Locate platelets.
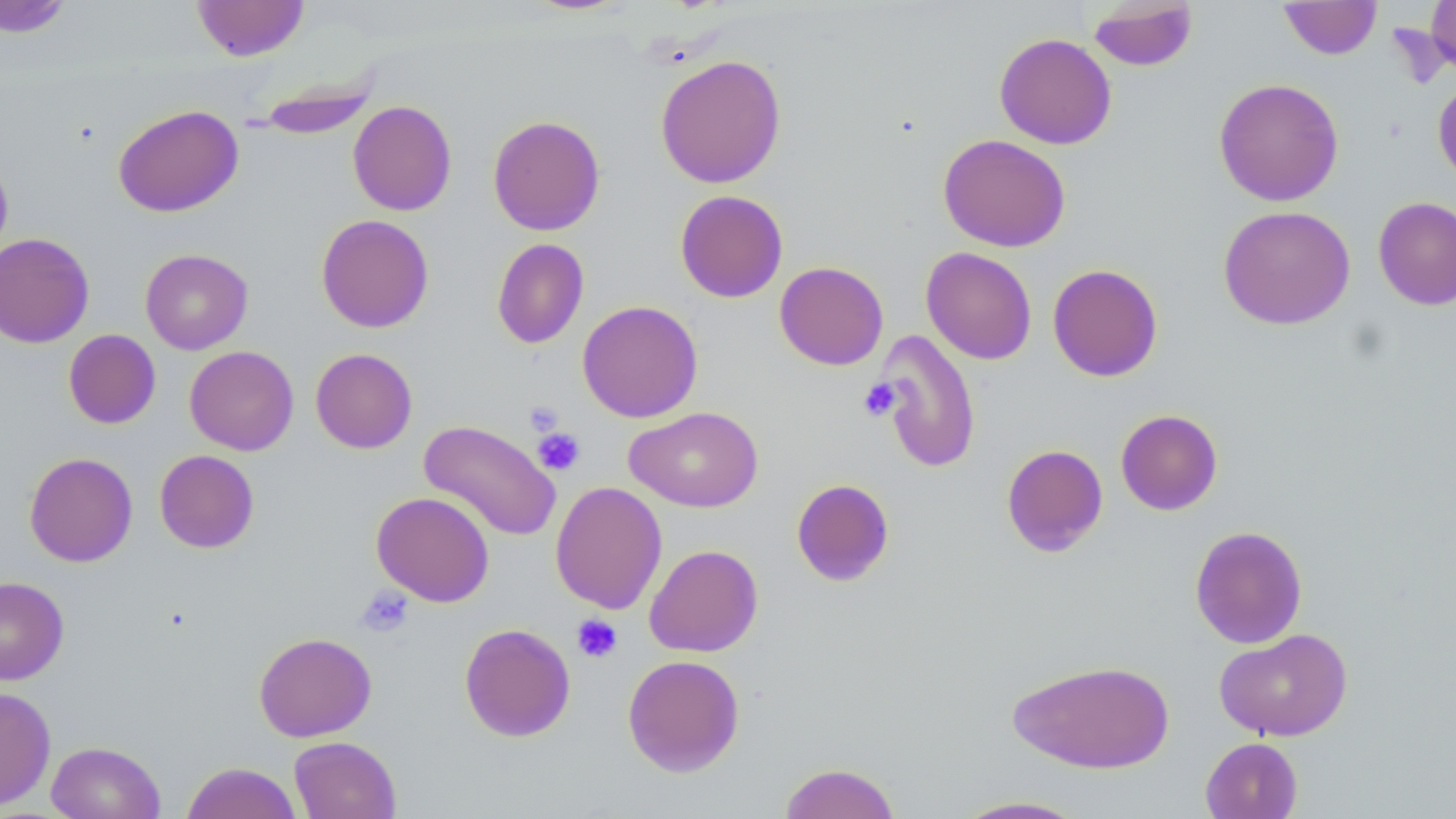

Approximate bounding boxes as [x1, y1, x2, y2] in pixels.
Platelets: [859, 378, 901, 422], [525, 401, 564, 437], [533, 427, 585, 476], [356, 585, 414, 636], [572, 613, 622, 663].

{
  "slide_level_diagnosis": "negative for blood parasites",
  "stain": "May-Grünwald-Giemsa",
  "uninfected_red_blood_cell_locations": "approximate bounding boxes as [x1, y1, x2, y2] in pixels: [0, 0, 73, 38], [192, 0, 309, 61], [1088, 0, 1199, 72], [1426, 0, 1456, 78], [1279, 1, 1382, 60], [994, 32, 1117, 149], [655, 54, 786, 188], [247, 69, 382, 139], [1433, 77, 1456, 187], [1214, 78, 1344, 206], [347, 100, 457, 216], [113, 104, 243, 217], [487, 114, 605, 236], [938, 133, 1071, 252], [0, 150, 13, 264], [674, 190, 788, 302], [1373, 195, 1456, 311], [1218, 205, 1356, 330], [316, 214, 434, 333], [0, 233, 94, 348], [491, 238, 589, 348], [921, 247, 1037, 364], [140, 249, 253, 355], [774, 261, 888, 370], [1047, 263, 1163, 382], [577, 300, 703, 423], [63, 329, 161, 429], [872, 329, 983, 474], [184, 346, 299, 455], [310, 348, 417, 453], [625, 406, 763, 512], [1115, 409, 1223, 515], [418, 419, 561, 542], [1002, 444, 1109, 557], [154, 450, 259, 553], [24, 452, 138, 567], [791, 478, 895, 586], [550, 481, 667, 615], [371, 491, 494, 606], [1189, 525, 1308, 648], [644, 544, 763, 657], [0, 577, 69, 685], [459, 623, 576, 742], [1214, 628, 1353, 741], [253, 632, 377, 742], [622, 654, 745, 777], [1007, 658, 1175, 774], [0, 686, 56, 810], [289, 736, 401, 819], [1200, 737, 1303, 819], [46, 741, 165, 819], [181, 761, 303, 819], [778, 762, 902, 819], [949, 795, 1091, 818]",
  "field_of_view": "one of a larger specimen",
  "image_size": "1456×819 pixels",
  "magnification": "1000x",
  "preparation": "thin blood smear",
  "modality": "optical microscopy"
}